Locate every leukocyte (white blood cell).
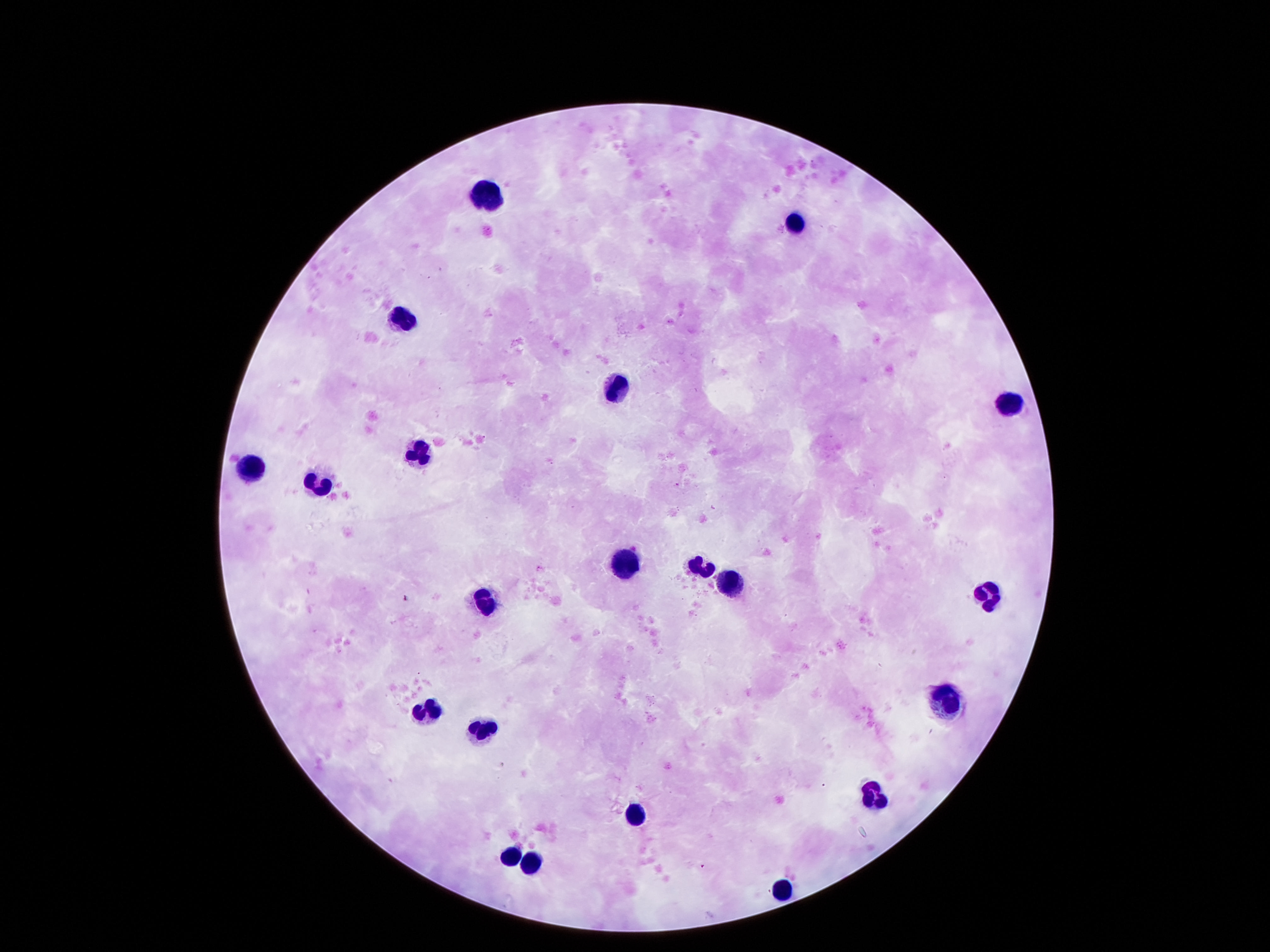
Approximate centers as [x, y] in pixels.
Leukocytes: [487, 192], [791, 219], [403, 318], [617, 385], [1007, 403], [421, 450], [253, 465], [319, 484], [623, 556], [698, 565], [731, 583], [986, 594], [481, 601], [944, 700], [427, 711], [481, 727], [872, 793], [641, 810], [508, 856], [526, 862], [785, 885].

Summary:
  - Capture: smartphone camera through the microscope eyepiece
  - Magnification: 100x
  - Preparation: thick peripheral-blood smear
  - Field of view: one from this slide
  - Patient malaria status: negative
  - Stain: Giemsa
  - Image size: 1270×952 pixels